State which parasite is depicted.
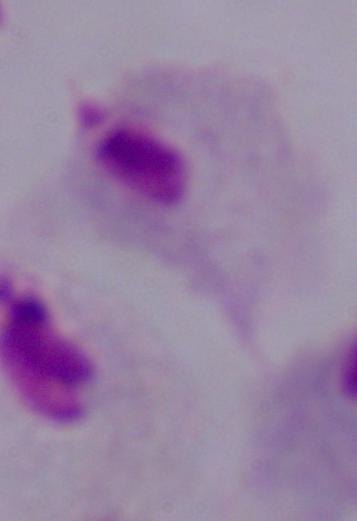
A trichomonad.

1000x magnification. Micrograph.